Assess this cell for malaria.
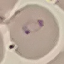

It is parasitized.

Thin blood film. Giemsa-stained preparation. Cell patch, automatically extracted from a larger field of view and resized to 64 × 64 pixels. Acquired by smartphone through the microscope eyepiece.